Describe the morphology of the red blood cells.
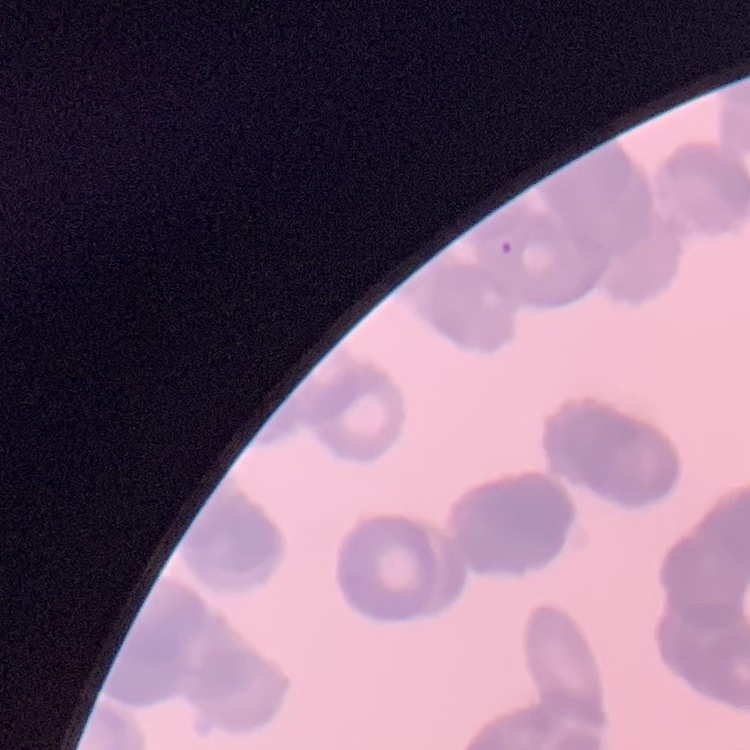

Rouleaux formation.

Summary:
  - Preparation: thin blood smear
  - Stain: Field's or Giemsa
  - Image type: square crop of a larger photomicrograph